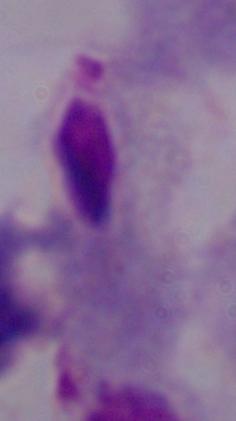
Summary:
  - Modality: photomicrograph
  - Identification: trichomonad
  - Magnification: 1000x